Comment on the morphology of the erythrocytes.
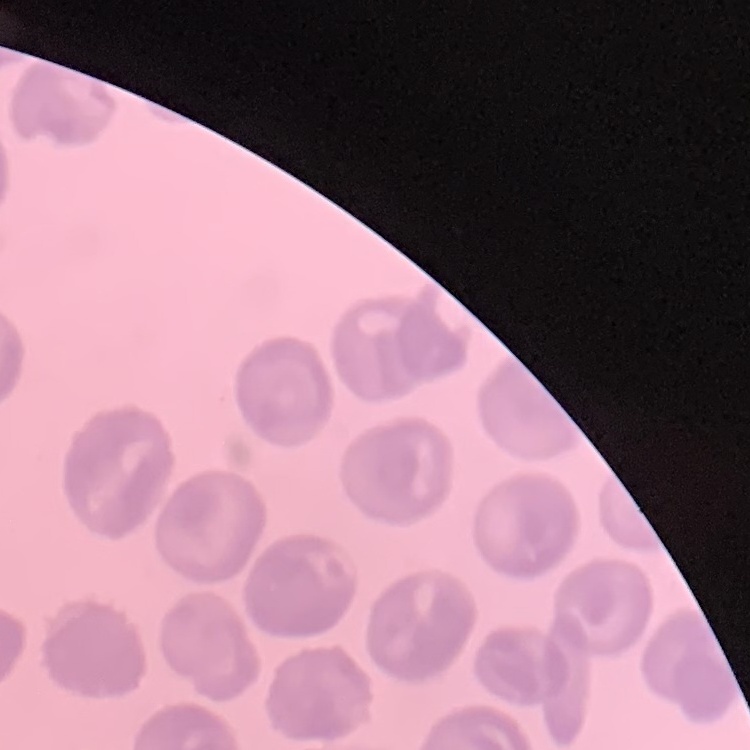
No rouleaux formation.

Field's or Giemsa stain. Square crop of a larger photomicrograph. Thin peripheral smear.